Identify the blood parasite species.
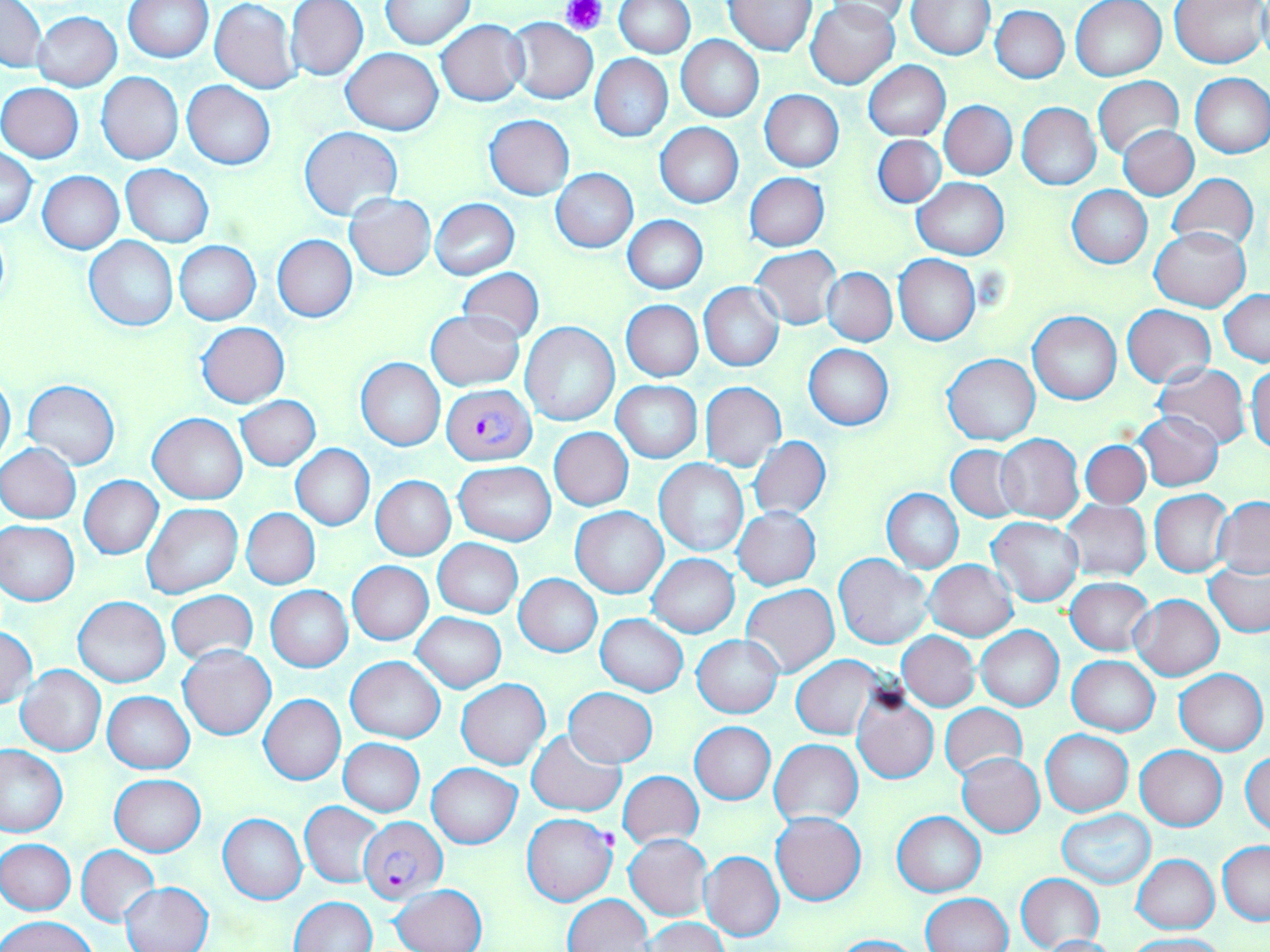
Plasmodium falciparum.

Approximate bounding boxes as (x1, y1, x2, y2) in pixels. Plasmodium falciparum-infected red blood cell locations: (441, 384, 534, 465), (521, 812, 618, 906), (358, 816, 446, 903). Uninfected red blood cell locations: (0, 0, 46, 72), (124, 0, 213, 63), (286, 0, 368, 81), (613, 0, 695, 58), (907, 0, 993, 59), (1071, 0, 1167, 81), (1172, 0, 1268, 67), (210, 1, 300, 94), (380, 1, 475, 49), (724, 1, 817, 55), (807, 1, 900, 89), (822, 1, 916, 28), (990, 5, 1069, 83), (32, 11, 122, 91), (506, 18, 597, 103), (436, 19, 529, 106), (676, 35, 763, 122), (341, 48, 443, 134), (591, 55, 673, 141), (864, 60, 951, 141), (97, 72, 183, 164), (1190, 73, 1270, 158), (1093, 76, 1184, 160), (182, 80, 274, 169), (1, 83, 84, 162), (760, 90, 844, 171), (931, 100, 1012, 259), (940, 101, 1016, 180), (1017, 103, 1101, 190), (485, 116, 574, 199), (656, 123, 743, 207), (1119, 125, 1198, 199), (299, 126, 402, 220), (873, 135, 945, 208), (1, 148, 38, 228), (120, 164, 213, 247), (551, 168, 637, 253), (38, 171, 124, 253), (745, 173, 829, 251), (1167, 173, 1258, 253), (912, 178, 1009, 259), (1067, 186, 1151, 268), (345, 193, 436, 280), (431, 198, 518, 279), (623, 215, 707, 293), (1150, 226, 1251, 312), (85, 236, 178, 330), (272, 236, 356, 322), (174, 240, 261, 324), (751, 246, 842, 329), (893, 254, 981, 346), (822, 268, 897, 346), (458, 269, 543, 344), (699, 282, 785, 372), (1220, 289, 1270, 366), (622, 300, 702, 381), (1122, 306, 1216, 387), (1027, 310, 1121, 404), (426, 311, 525, 390), (197, 322, 288, 408), (519, 322, 619, 427), (804, 344, 894, 430), (942, 354, 1040, 445), (357, 358, 445, 449), (1153, 363, 1251, 449), (1247, 363, 1269, 454), (0, 372, 16, 466), (22, 379, 120, 469), (612, 380, 702, 463), (700, 382, 786, 471), (236, 395, 320, 471), (1136, 411, 1223, 491), (149, 413, 246, 504), (550, 428, 634, 510), (995, 434, 1084, 523), (749, 436, 830, 522), (1081, 440, 1151, 508), (0, 443, 81, 523), (946, 443, 1024, 521), (291, 444, 374, 530), (655, 460, 748, 557), (454, 462, 555, 546), (79, 475, 163, 559), (371, 476, 455, 560), (883, 488, 963, 572), (1151, 490, 1234, 578), (1214, 498, 1270, 577), (1061, 500, 1151, 580), (143, 503, 242, 599), (570, 506, 668, 598), (732, 506, 821, 590), (242, 508, 319, 589), (987, 516, 1084, 606), (0, 521, 79, 606), (434, 538, 523, 618), (835, 553, 933, 649), (647, 554, 740, 636), (925, 561, 1018, 640), (347, 562, 433, 644), (1205, 563, 1270, 638), (514, 574, 602, 657), (1065, 577, 1152, 655), (741, 585, 839, 677), (266, 586, 353, 671), (166, 591, 259, 666), (1130, 594, 1223, 681), (73, 596, 170, 687), (412, 612, 507, 693), (596, 615, 688, 695), (0, 626, 38, 708), (976, 626, 1063, 711), (897, 631, 979, 710), (692, 635, 783, 718), (180, 645, 275, 739), (1067, 655, 1160, 735), (347, 656, 445, 743), (791, 657, 882, 738), (15, 665, 107, 756), (1175, 669, 1268, 755), (456, 679, 551, 770), (851, 686, 939, 784), (564, 688, 657, 766), (103, 691, 194, 773), (259, 694, 346, 786), (940, 703, 1027, 781), (690, 721, 776, 804), (528, 730, 624, 816), (1040, 730, 1133, 816), (339, 738, 425, 816), (770, 739, 863, 827), (0, 744, 67, 837), (1135, 746, 1227, 830), (957, 752, 1045, 836), (1242, 754, 1270, 835), (427, 763, 521, 848), (618, 770, 703, 848), (109, 775, 206, 856), (300, 801, 385, 888), (1058, 810, 1156, 889), (894, 811, 986, 896), (218, 813, 306, 905), (770, 813, 867, 906), (624, 834, 712, 920), (1, 839, 75, 915), (1218, 842, 1270, 924), (75, 845, 159, 926), (699, 850, 784, 942), (1133, 855, 1219, 933), (1015, 873, 1105, 951), (121, 881, 214, 952), (392, 884, 487, 952), (920, 893, 1013, 952), (563, 894, 652, 951), (292, 897, 376, 951), (2, 915, 98, 952), (644, 918, 727, 952), (1126, 933, 1229, 952), (830, 935, 926, 952), (1039, 935, 1118, 952). Platelet locations: (561, 0, 606, 36). Image is 1270×952 pixels. Captured at 1000x magnification. One field of a larger specimen. Optical microscopy. May-Grünwald-Giemsa stain. Thin blood film.